Assess this cell for malaria.
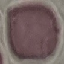
Uninfected.

Summary:
  - Image type: cell patch, automatically extracted from a larger field of view and resized to 64 × 64 pixels
  - Preparation: thin blood smear
  - Stain: Giemsa
  - Capture: smartphone camera at the microscope eyepiece